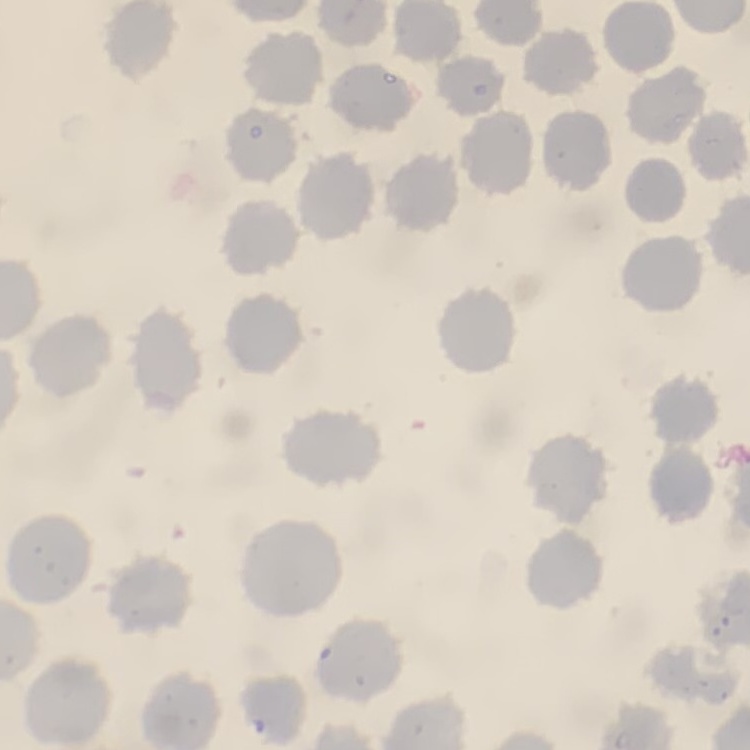
Summary:
  - Red blood cell morphology: no rouleaux formation
  - Image type: square crop of a larger photomicrograph
  - Stain: Field's or Giemsa
  - Preparation: thin blood smear